Describe the morphology of the red blood cells.
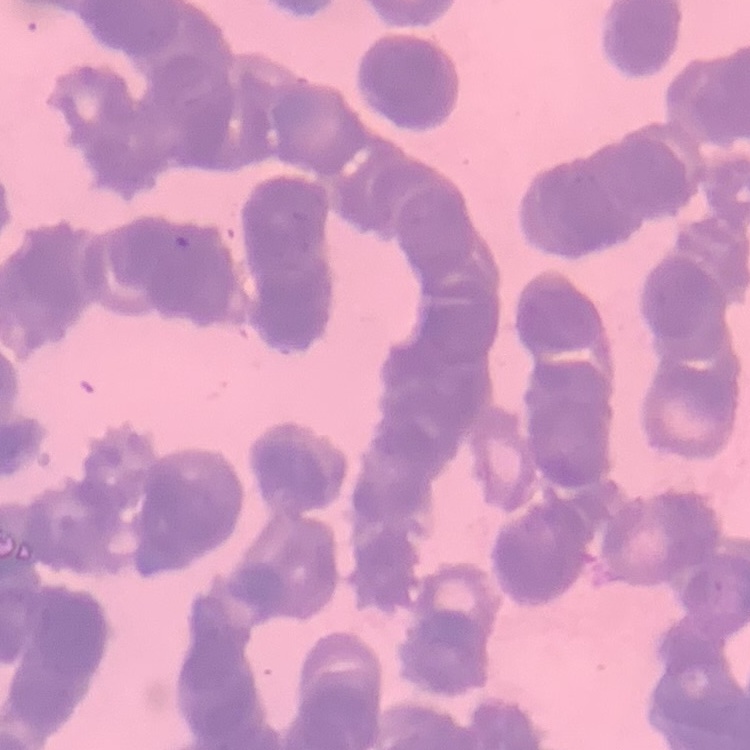

Rouleaux formation.

Summary:
  - Stain: Field's or Giemsa
  - Image type: one tile cut from a larger photomicrograph
  - Preparation: thin blood film